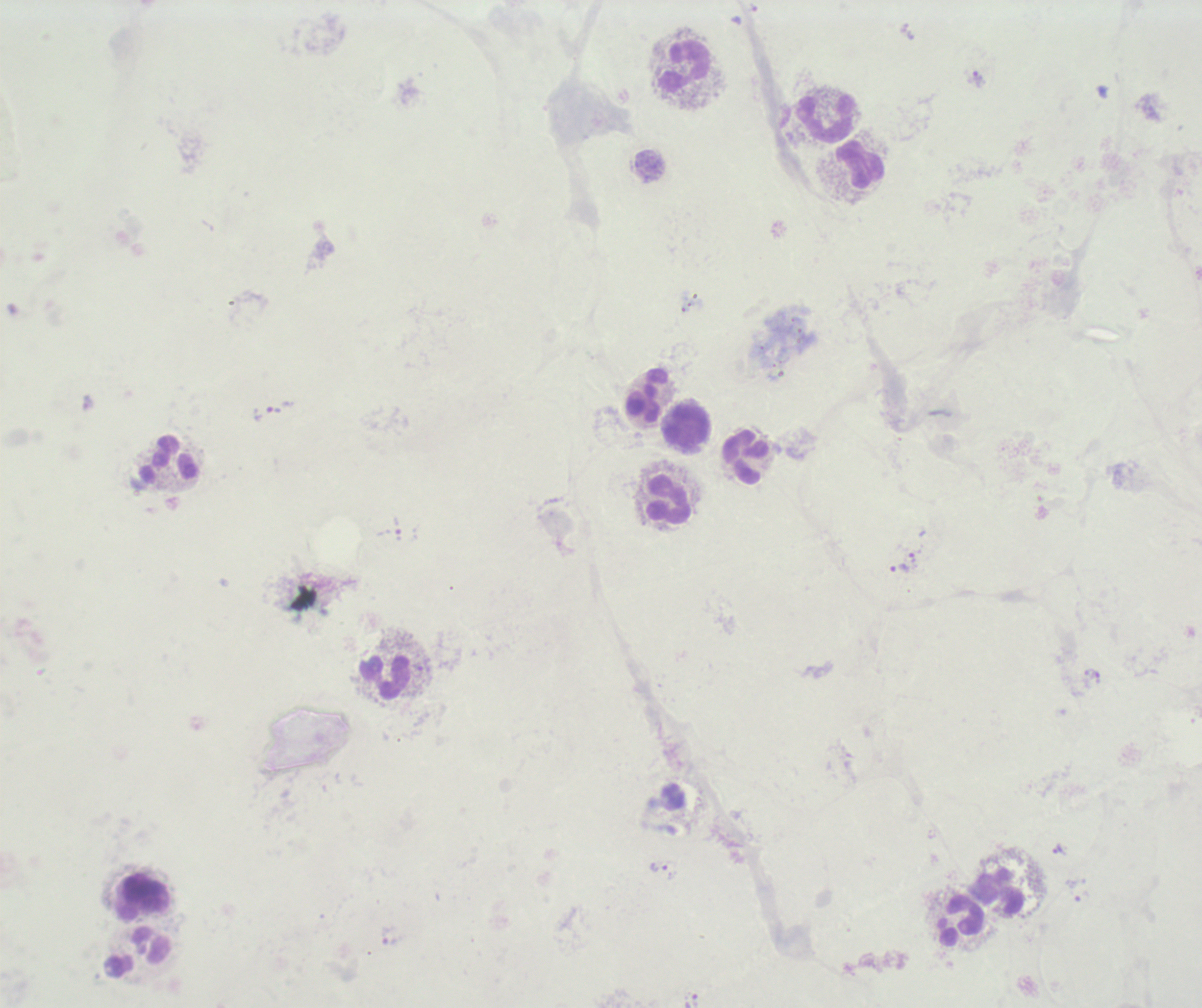
coordinate format = approximate centers as {x, y} in pixels
trophozoite locations = {976, 80}, {274, 411}, {397, 526}, {912, 559}, {900, 568}, {1058, 849}, {660, 867}
leukocyte locations = {684, 66}, {825, 117}, {860, 166}, {647, 395}, {686, 426}, {745, 456}, {170, 460}, {669, 500}, {384, 676}, {998, 894}, {142, 899}, {959, 922}, {138, 952}
field of view = single
result = malaria parasites identified
background quality = unsatisfactory
context = previously used in a real diagnosis
magnification = 100x
preparation = thick smear of blood
image size = 1202×1008 pixels
stain = Romanowsky